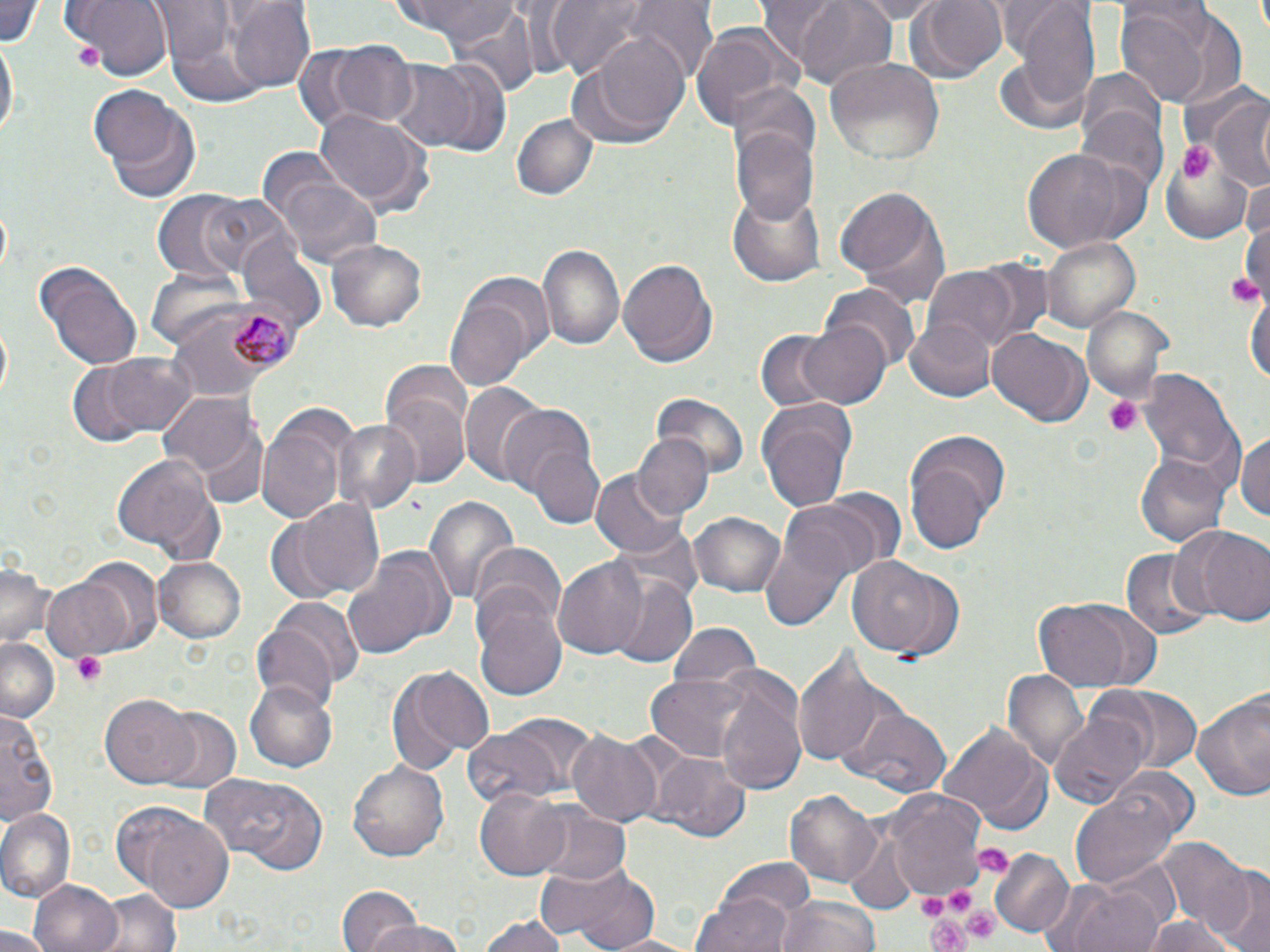 Approximate bounding boxes as named x1/y1/x2/y2 corners in pixels. Platelet locations: (x1=1179, y1=142, x2=1215, y2=181), (x1=1226, y1=268, x2=1262, y2=312), (x1=1102, y1=395, x2=1144, y2=437), (x1=70, y1=652, x2=108, y2=687), (x1=972, y1=843, x2=1013, y2=877), (x1=956, y1=901, x2=1005, y2=942), (x1=927, y1=911, x2=972, y2=952). Uninfected red blood cell locations: (x1=0, y1=0, x2=43, y2=49), (x1=68, y1=0, x2=171, y2=79), (x1=387, y1=0, x2=531, y2=46), (x1=546, y1=0, x2=658, y2=78), (x1=791, y1=0, x2=902, y2=91), (x1=847, y1=0, x2=948, y2=21), (x1=912, y1=0, x2=1007, y2=81), (x1=1113, y1=0, x2=1246, y2=111), (x1=628, y1=1, x2=719, y2=87), (x1=229, y1=2, x2=319, y2=91), (x1=1015, y1=3, x2=1100, y2=116), (x1=451, y1=10, x2=543, y2=99), (x1=694, y1=20, x2=805, y2=132), (x1=575, y1=36, x2=689, y2=145), (x1=1, y1=38, x2=16, y2=147), (x1=325, y1=40, x2=420, y2=128), (x1=826, y1=56, x2=944, y2=165), (x1=418, y1=58, x2=516, y2=158), (x1=390, y1=62, x2=480, y2=150), (x1=1075, y1=68, x2=1164, y2=165), (x1=726, y1=81, x2=819, y2=167), (x1=91, y1=86, x2=203, y2=202), (x1=1202, y1=88, x2=1270, y2=189), (x1=314, y1=107, x2=428, y2=212), (x1=1075, y1=107, x2=1168, y2=201), (x1=511, y1=113, x2=596, y2=200), (x1=732, y1=119, x2=818, y2=223), (x1=1019, y1=146, x2=1142, y2=254), (x1=1160, y1=156, x2=1252, y2=239), (x1=270, y1=166, x2=386, y2=272), (x1=1241, y1=179, x2=1270, y2=244), (x1=834, y1=185, x2=950, y2=308), (x1=728, y1=190, x2=825, y2=286), (x1=195, y1=192, x2=299, y2=281), (x1=155, y1=194, x2=244, y2=279), (x1=237, y1=230, x2=325, y2=328), (x1=326, y1=236, x2=427, y2=333), (x1=1040, y1=237, x2=1140, y2=332), (x1=536, y1=241, x2=625, y2=356), (x1=617, y1=255, x2=716, y2=366), (x1=37, y1=264, x2=141, y2=369), (x1=923, y1=266, x2=1024, y2=354), (x1=144, y1=270, x2=249, y2=352), (x1=1246, y1=282, x2=1269, y2=393), (x1=446, y1=285, x2=538, y2=391), (x1=823, y1=286, x2=919, y2=375), (x1=1084, y1=303, x2=1174, y2=408), (x1=799, y1=319, x2=892, y2=408), (x1=903, y1=319, x2=996, y2=402), (x1=989, y1=329, x2=1088, y2=426), (x1=757, y1=332, x2=836, y2=410), (x1=100, y1=351, x2=201, y2=439), (x1=66, y1=360, x2=163, y2=446), (x1=378, y1=365, x2=472, y2=483), (x1=1140, y1=367, x2=1243, y2=484), (x1=459, y1=383, x2=545, y2=486), (x1=158, y1=392, x2=258, y2=478), (x1=651, y1=392, x2=750, y2=481), (x1=755, y1=400, x2=857, y2=510), (x1=257, y1=405, x2=355, y2=522), (x1=511, y1=407, x2=603, y2=526), (x1=335, y1=420, x2=416, y2=513), (x1=1238, y1=426, x2=1270, y2=522), (x1=902, y1=428, x2=1009, y2=554), (x1=632, y1=433, x2=714, y2=518), (x1=1136, y1=452, x2=1230, y2=547), (x1=111, y1=454, x2=226, y2=562), (x1=592, y1=470, x2=687, y2=558), (x1=788, y1=489, x2=903, y2=578), (x1=422, y1=493, x2=518, y2=609), (x1=292, y1=498, x2=388, y2=599), (x1=688, y1=509, x2=785, y2=597), (x1=1177, y1=526, x2=1270, y2=628), (x1=758, y1=533, x2=851, y2=631), (x1=475, y1=542, x2=563, y2=631), (x1=342, y1=546, x2=454, y2=659), (x1=1119, y1=549, x2=1211, y2=638), (x1=845, y1=554, x2=963, y2=661), (x1=552, y1=556, x2=650, y2=657), (x1=153, y1=557, x2=245, y2=643), (x1=39, y1=576, x2=139, y2=661), (x1=608, y1=577, x2=696, y2=669), (x1=471, y1=590, x2=567, y2=703), (x1=1031, y1=597, x2=1160, y2=695), (x1=271, y1=598, x2=364, y2=693), (x1=251, y1=620, x2=340, y2=709), (x1=666, y1=623, x2=762, y2=692), (x1=1, y1=638, x2=60, y2=722), (x1=794, y1=643, x2=894, y2=769), (x1=387, y1=664, x2=493, y2=773), (x1=1002, y1=668, x2=1086, y2=769), (x1=645, y1=676, x2=753, y2=760), (x1=245, y1=680, x2=337, y2=772), (x1=717, y1=680, x2=810, y2=795), (x1=1093, y1=686, x2=1202, y2=772), (x1=1193, y1=686, x2=1270, y2=801), (x1=101, y1=694, x2=200, y2=788), (x1=841, y1=706, x2=951, y2=795), (x1=1049, y1=707, x2=1150, y2=808), (x1=1, y1=708, x2=58, y2=830), (x1=152, y1=708, x2=243, y2=795), (x1=494, y1=713, x2=598, y2=795), (x1=939, y1=721, x2=1051, y2=831), (x1=462, y1=730, x2=564, y2=810), (x1=567, y1=730, x2=664, y2=826), (x1=657, y1=755, x2=752, y2=843), (x1=348, y1=759, x2=450, y2=862), (x1=1113, y1=764, x2=1198, y2=836), (x1=198, y1=774, x2=325, y2=871), (x1=473, y1=786, x2=571, y2=878), (x1=785, y1=788, x2=882, y2=889), (x1=1070, y1=790, x2=1179, y2=891), (x1=887, y1=792, x2=986, y2=895), (x1=532, y1=805, x2=631, y2=887), (x1=1, y1=807, x2=76, y2=899), (x1=117, y1=807, x2=237, y2=908), (x1=841, y1=828, x2=918, y2=913), (x1=1154, y1=839, x2=1250, y2=930), (x1=990, y1=850, x2=1076, y2=939), (x1=706, y1=857, x2=815, y2=935), (x1=537, y1=861, x2=663, y2=951), (x1=1208, y1=865, x2=1270, y2=952), (x1=27, y1=879, x2=124, y2=952), (x1=1064, y1=882, x2=1168, y2=952), (x1=93, y1=888, x2=183, y2=952), (x1=337, y1=888, x2=420, y2=952), (x1=692, y1=892, x2=795, y2=952), (x1=777, y1=896, x2=882, y2=952), (x1=479, y1=911, x2=566, y2=952), (x1=1142, y1=915, x2=1240, y2=952), (x1=361, y1=916, x2=470, y2=952), (x1=0, y1=927, x2=52, y2=952), (x1=602, y1=932, x2=696, y2=951). Plasmodium malariae-infected red blood cell locations: (x1=181, y1=298, x2=301, y2=386). Slide-level diagnosis: Plasmodium malariae. Single field of view. Optical microscopy. 1000x magnification. Thin blood smear. Image is 1270×952 pixels. May-Grünwald-Giemsa stain.